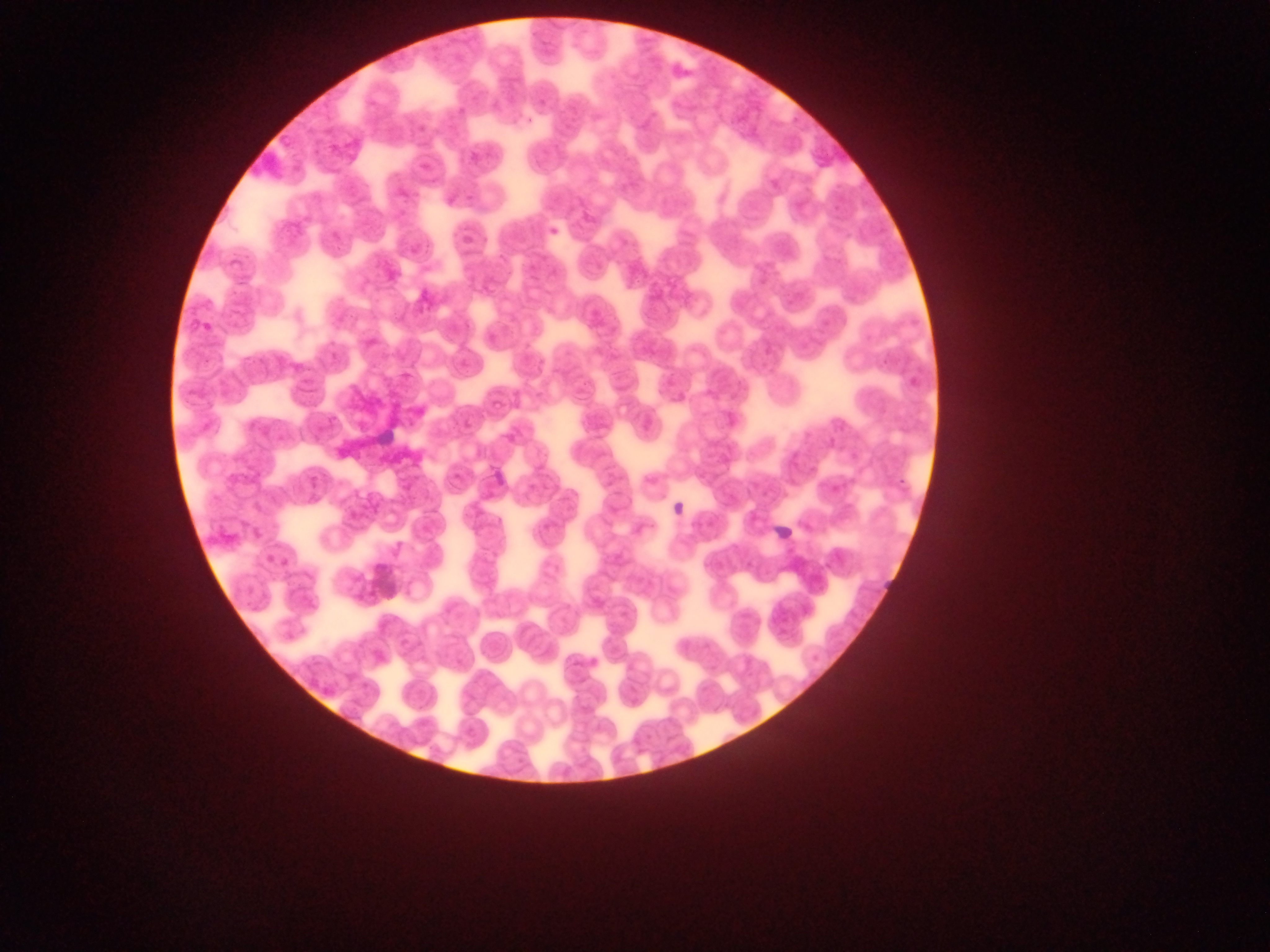
{
  "preparation": "thin blood smear",
  "country": "Ghana",
  "plasmodium_parasite_locations": "approximate bounding boxes as {left, top, right, bottom} in pixels: {454, 101, 474, 127}, {548, 225, 575, 246}, {487, 466, 508, 489}, {671, 499, 691, 519}, {771, 522, 797, 547}, {884, 574, 901, 597}",
  "field_of_view": "single",
  "capture": "mobile-phone photograph through a microscope",
  "image_size": "1270×952 pixels"
}